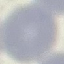
Summary:
  - Result: negative for malaria parasites
  - Image type: automatically extracted cell patch, resized to 64 × 64 pixels
  - Stain: Giemsa
  - Preparation: thin blood film
  - Capture: smartphone through the microscope eyepiece